Classify this cell by malaria status.
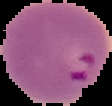

It is parasitized.

{
  "image_type": "segmented cell region with the area outside set to black",
  "preparation": "thin blood smear",
  "image_size": "112×106 pixels"
}